Report the malaria status of this cell.
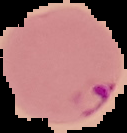
Parasitized.

Summary:
  - Preparation: thin blood film
  - Image size: 127×133 pixels
  - Image type: cell region segmented out of the field of view; surrounding area masked to black